Classify this cell by malaria status.
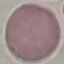
It is uninfected.

Summary:
  - Stain: Giemsa
  - Preparation: thin blood smear
  - Capture: smartphone camera at the microscope eyepiece
  - Image type: cell patch, automatically extracted from a larger field of view and resized to 64 × 64 pixels